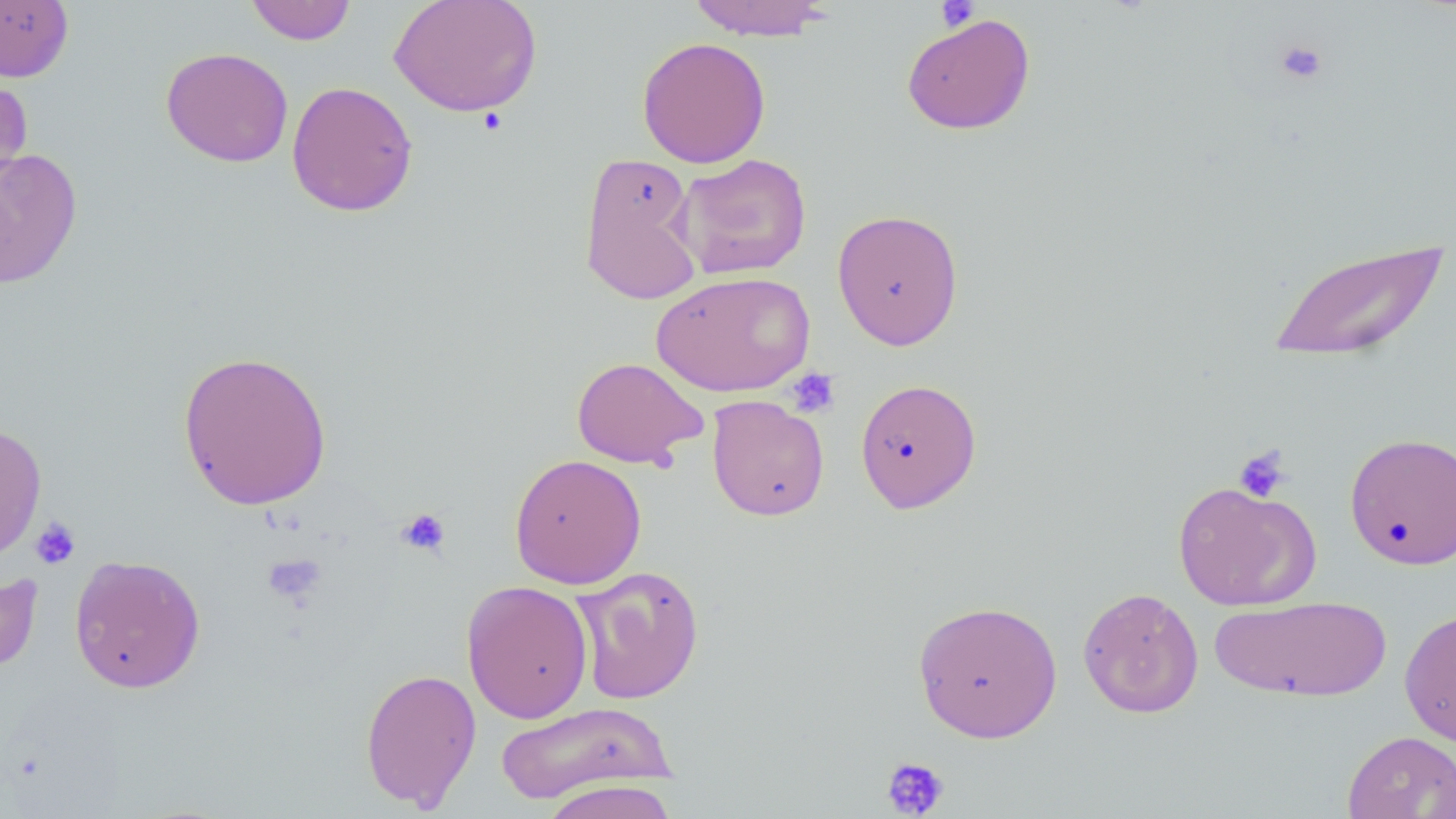
slide_level_diagnosis: no evidence of blood parasites
modality: light microscopy
magnification: 1000x
platelet_locations: 'approximate bounding boxes as (x1,y1)-(x2,y2) corner pairs in pixels: (936,1)-(980,33), (1274,39)-(1328,86), (785,368)-(840,418), (1233,446)-(1291,502), (395,507)-(451,558), (30,517)-(81,570), (261,554)-(326,606), (881,756)-(950,817)'
uninfected_red_blood_cell_locations: 'approximate bounding boxes as (x1,y1)-(x2,y2) corner pairs in pixels: (245,0)-(357,45), (388,0)-(543,117), (685,0)-(835,41), (0,1)-(74,82), (901,13)-(1036,135), (636,36)-(771,168), (160,46)-(293,168), (0,70)-(34,203), (286,81)-(418,217), (0,147)-(83,289), (577,152)-(704,307), (674,153)-(812,279), (831,208)-(964,350), (1267,236)-(1447,365), (651,271)-(817,397), (177,349)-(333,511), (571,357)-(707,469), (855,378)-(982,514), (706,395)-(830,521), (0,422)-(46,562), (1344,431)-(1456,570), (509,454)-(647,589), (1172,481)-(1322,611), (69,554)-(206,693), (571,565)-(705,705), (0,569)-(43,675), (461,579)-(593,724), (1077,586)-(1204,718), (1210,595)-(1392,703), (912,599)-(1063,742), (1399,606)-(1456,748), (360,667)-(482,811), (493,702)-(676,805), (1342,730)-(1456,819), (538,780)-(680,819)'
image_size: 1456×819 pixels
field_of_view: one of a larger specimen
preparation: thin blood film
stain: May-Grünwald-Giemsa